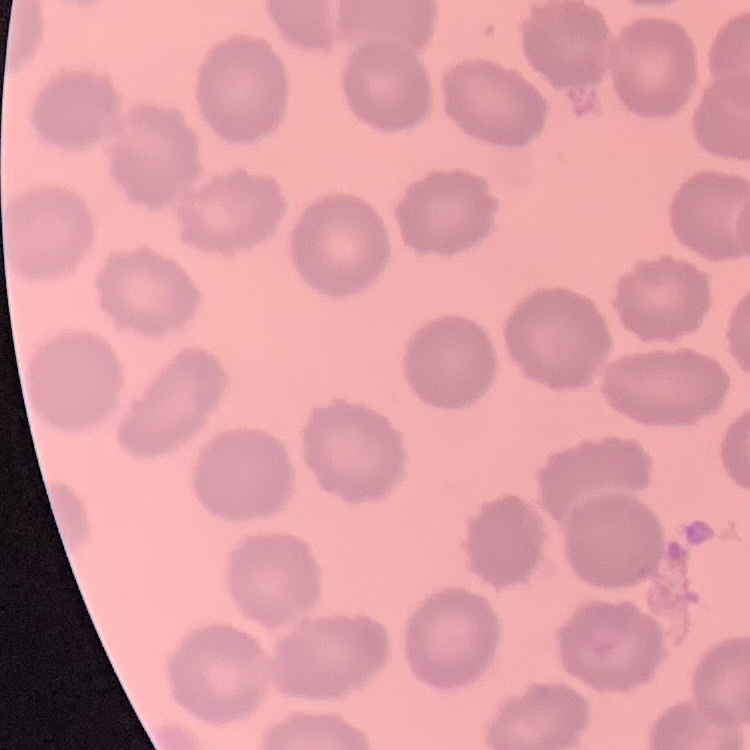
{
  "erythrocyte_morphology": "no rouleaux formation",
  "image_type": "one tile cut from a larger photomicrograph",
  "preparation": "thin peripheral smear",
  "stain": "Field's or Giemsa"
}